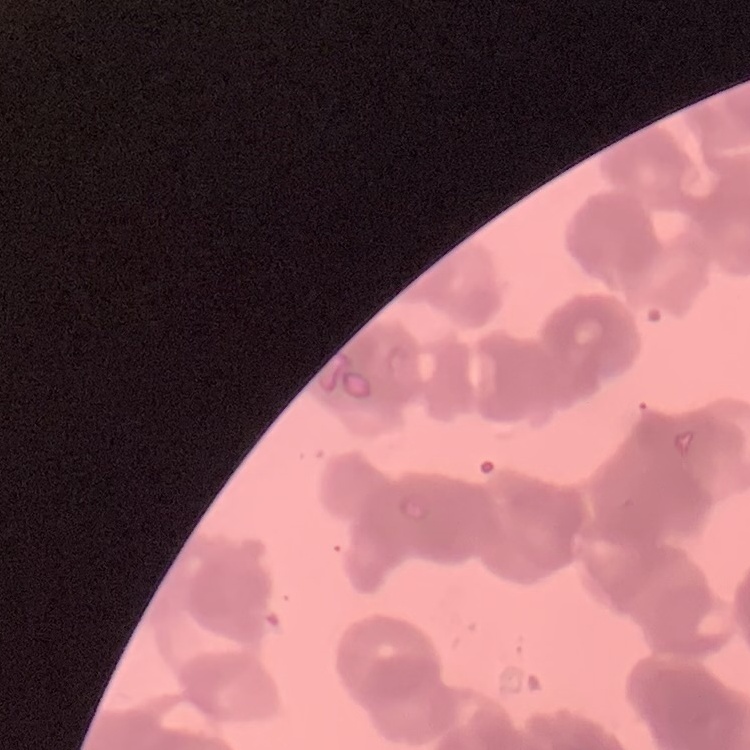
The erythrocytes exhibit rouleaux formation. Thin blood film. Square crop of a larger photomicrograph. Stained with either Field's or Giemsa.